Comment on the morphology of the erythrocytes.
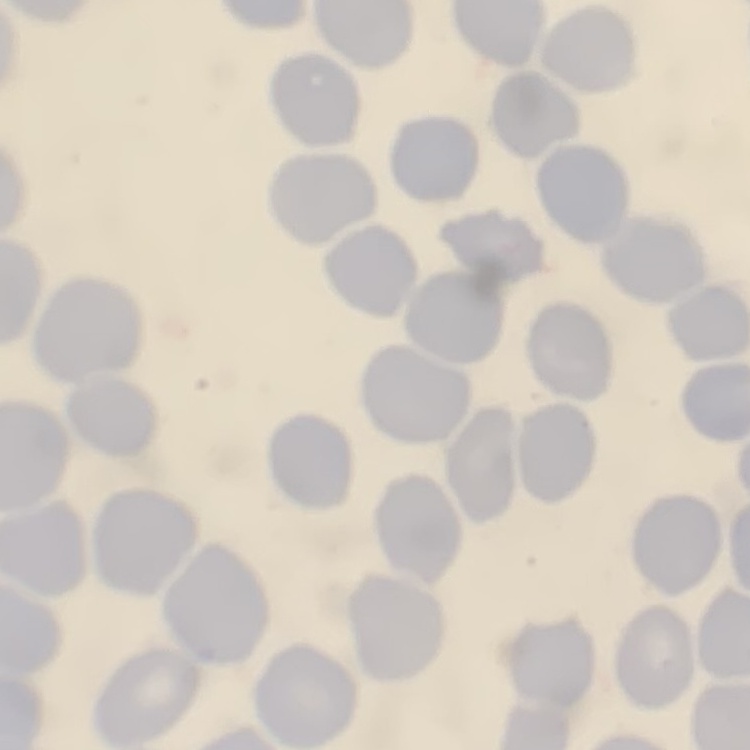

They show no rouleaux formation.

Summary:
  - Image type: square crop of a larger photomicrograph
  - Preparation: thin peripheral smear
  - Stain: Field's or Giemsa